Classify this cell by malaria status.
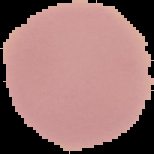

Uninfected.

image_size: 154×154 pixels
preparation: thin blood smear
image_type: cell region segmented out of the field of view; surrounding area masked to black